Identify the preparation type.
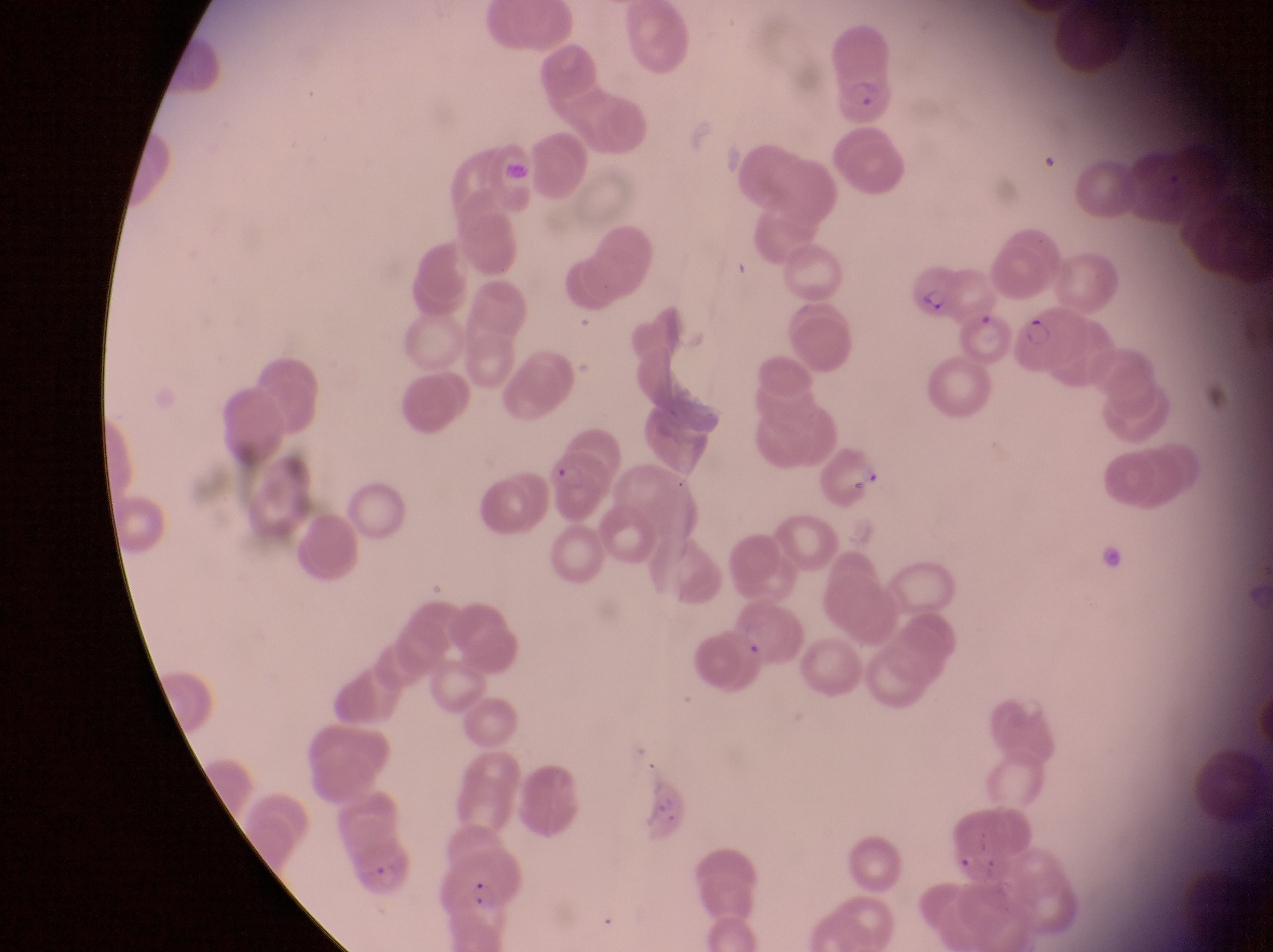

Thin blood smear.

Approximate bounding boxes as (left, top, right, bottom) in pixels. Parasitised red blood cell locations: (825, 31, 899, 125), (911, 257, 963, 329), (1016, 300, 1086, 378), (970, 312, 1015, 369), (817, 439, 887, 514), (546, 447, 616, 522), (729, 597, 809, 672), (354, 836, 419, 904), (442, 852, 532, 920). Image is 1273×952 pixels. Single field of view. Collected in Uganda. Captured by a smartphone held over the eyepiece of an Olympus CX-23 microscope. Magnification of 1000x.